Locate every blood parasite and identify its species.
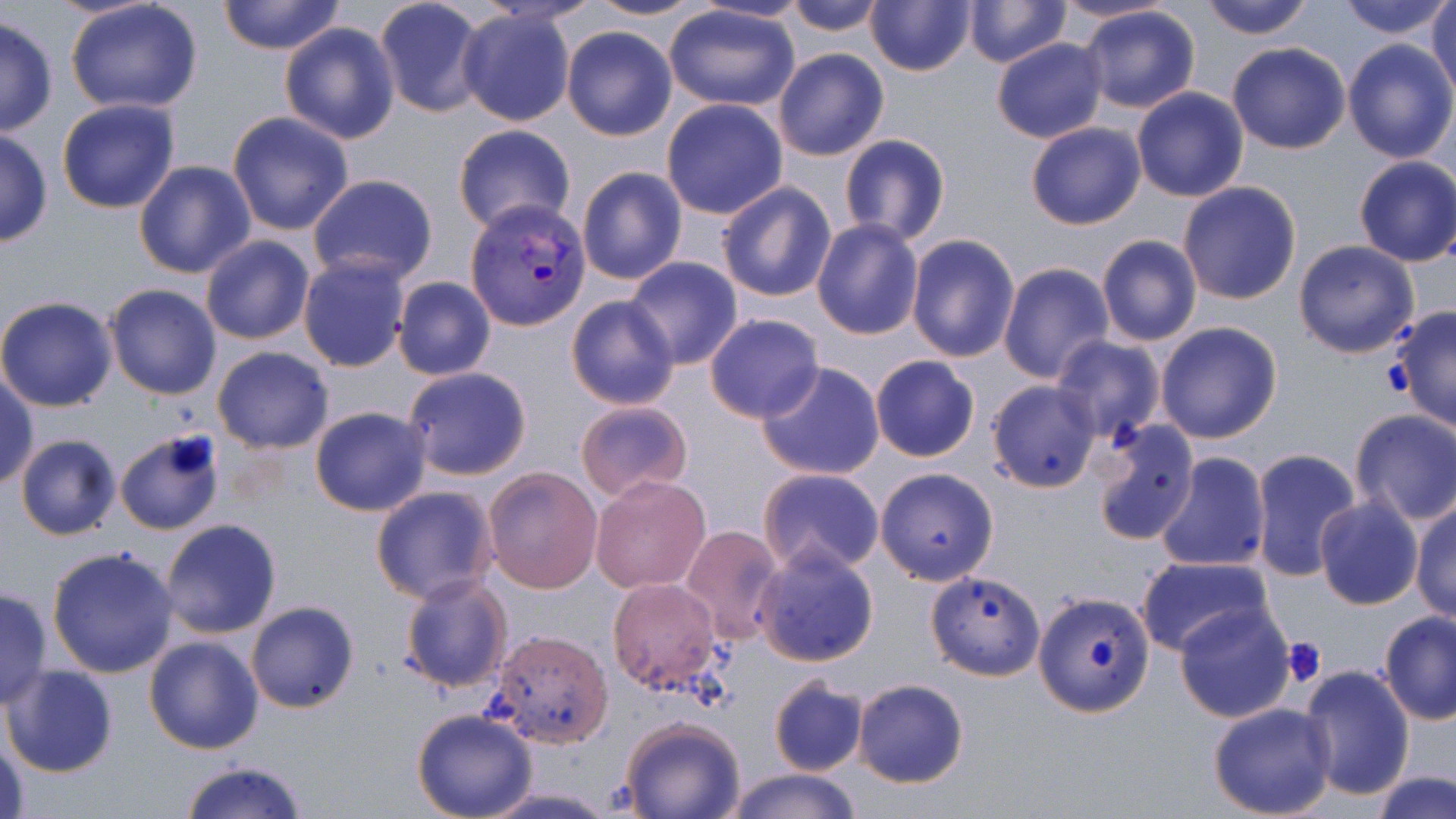
Approximate bounding boxes as [x1, y1, x2, y2] in pixels.
Plasmodium vivax-infected red blood cells: [465, 199, 590, 328].
No Plasmodium falciparum, Plasmodium ovale, Plasmodium malariae, Babesia divergens, or Trypanosoma brucei observed.

Uninfected red blood cell locations: [65, 0, 205, 114], [217, 0, 345, 55], [374, 0, 490, 119], [583, 0, 711, 21], [784, 0, 890, 36], [866, 0, 976, 77], [962, 0, 1071, 67], [1050, 0, 1179, 26], [1199, 0, 1315, 39], [1337, 0, 1454, 39], [1429, 0, 1456, 102], [662, 4, 801, 112], [1079, 5, 1200, 112], [456, 10, 576, 126], [0, 16, 58, 138], [278, 21, 400, 144], [561, 25, 678, 140], [991, 37, 1107, 144], [1343, 39, 1456, 164], [1227, 42, 1351, 154], [773, 48, 889, 161], [1131, 87, 1248, 203], [661, 98, 788, 219], [56, 99, 181, 215], [226, 112, 354, 236], [452, 123, 576, 236], [1026, 123, 1146, 230], [0, 127, 52, 248], [839, 135, 950, 246], [1353, 155, 1456, 267], [132, 161, 255, 279], [577, 166, 687, 284], [307, 173, 439, 286], [716, 181, 836, 303], [1178, 181, 1302, 305], [811, 218, 925, 338], [1096, 234, 1203, 347], [200, 235, 315, 346], [905, 235, 1019, 362], [1292, 239, 1420, 359], [297, 253, 411, 373], [625, 256, 745, 370], [997, 261, 1114, 383], [392, 276, 496, 381], [104, 283, 223, 400], [564, 294, 681, 410], [0, 295, 119, 413], [1390, 306, 1456, 432], [704, 313, 824, 423], [1155, 321, 1284, 443], [1052, 335, 1165, 443], [212, 347, 335, 453], [869, 355, 980, 462], [756, 361, 885, 481], [401, 365, 533, 481], [0, 373, 37, 490], [985, 380, 1103, 494], [574, 399, 694, 504], [309, 406, 431, 515], [1349, 408, 1456, 525], [1093, 417, 1200, 544], [114, 429, 226, 536], [15, 433, 123, 542], [1247, 448, 1362, 583], [1152, 453, 1271, 573], [481, 465, 602, 593], [874, 466, 1001, 586], [758, 467, 885, 576], [589, 473, 712, 595], [370, 485, 499, 605], [1315, 496, 1423, 611], [706, 499, 831, 626], [1410, 499, 1455, 623], [160, 518, 283, 640], [681, 524, 786, 645], [46, 545, 180, 681], [756, 547, 880, 668], [1135, 554, 1273, 657], [924, 569, 1046, 682], [398, 574, 514, 693], [606, 577, 725, 697], [0, 587, 54, 709], [1033, 591, 1155, 717], [245, 600, 359, 713], [1173, 600, 1295, 723], [1378, 612, 1455, 726], [486, 629, 614, 748], [144, 635, 266, 754], [2, 664, 120, 778], [1297, 665, 1415, 799], [768, 677, 869, 776], [851, 679, 969, 787], [1207, 701, 1337, 819], [412, 709, 539, 819], [619, 718, 745, 819], [1, 735, 32, 819], [177, 760, 310, 819], [722, 768, 862, 819], [1370, 771, 1455, 819], [477, 786, 621, 818]. Platelet locations: [1280, 636, 1326, 687]. Slide-level diagnosis: Plasmodium vivax. May-Grünwald-Giemsa stain. 1000x magnification. One field of a larger specimen. Optical microscopy. Image is 1456×819 pixels. Thin blood smear.